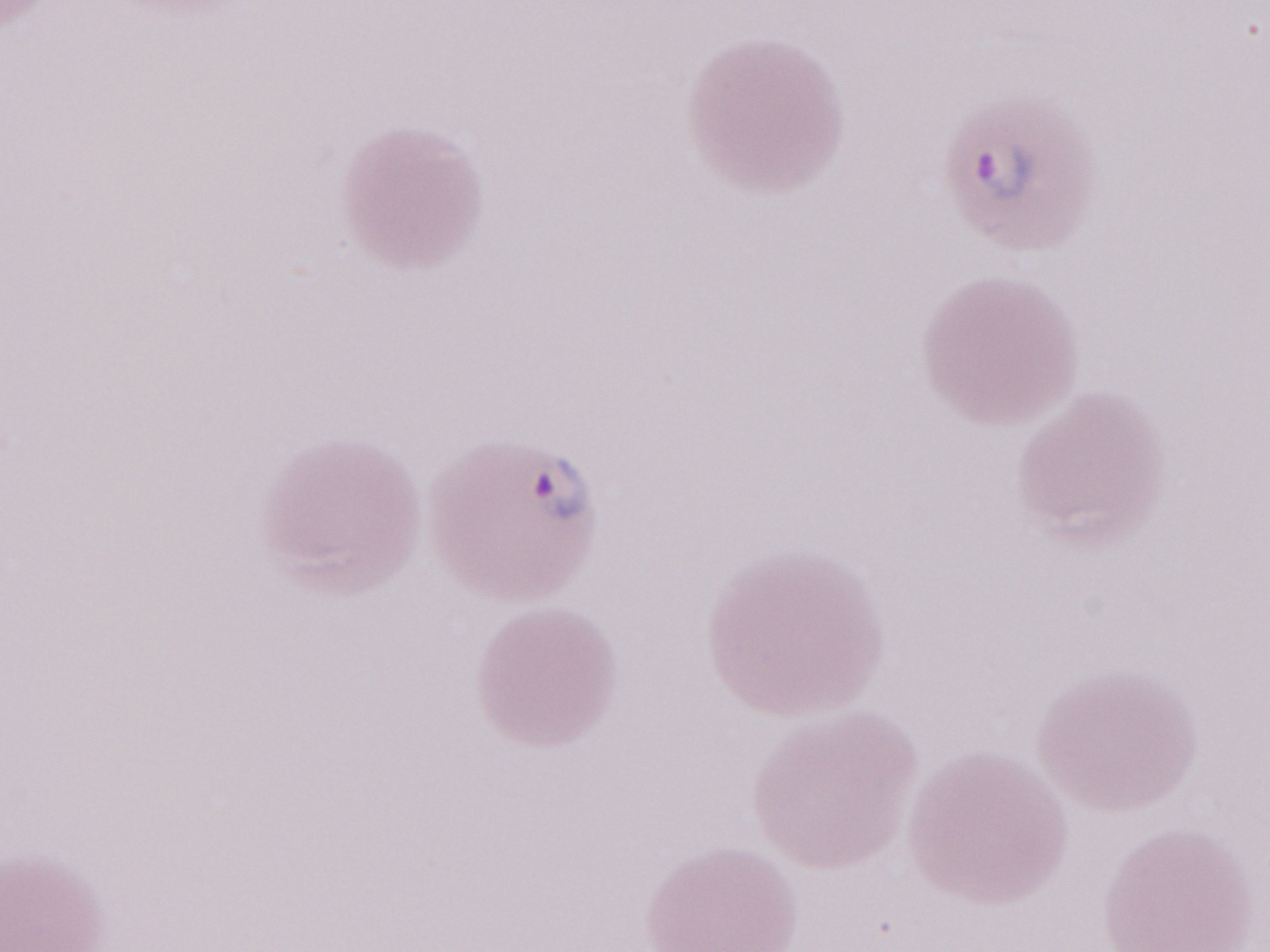

Image is 1270×952 pixels. May-Grünwald-Giemsa (MGG) stain. Thin blood film. Patient diagnosis: malaria infection. One field of this slide. Olympus BX43 microscope and DP73 digital camera. Magnification: 1,000x.